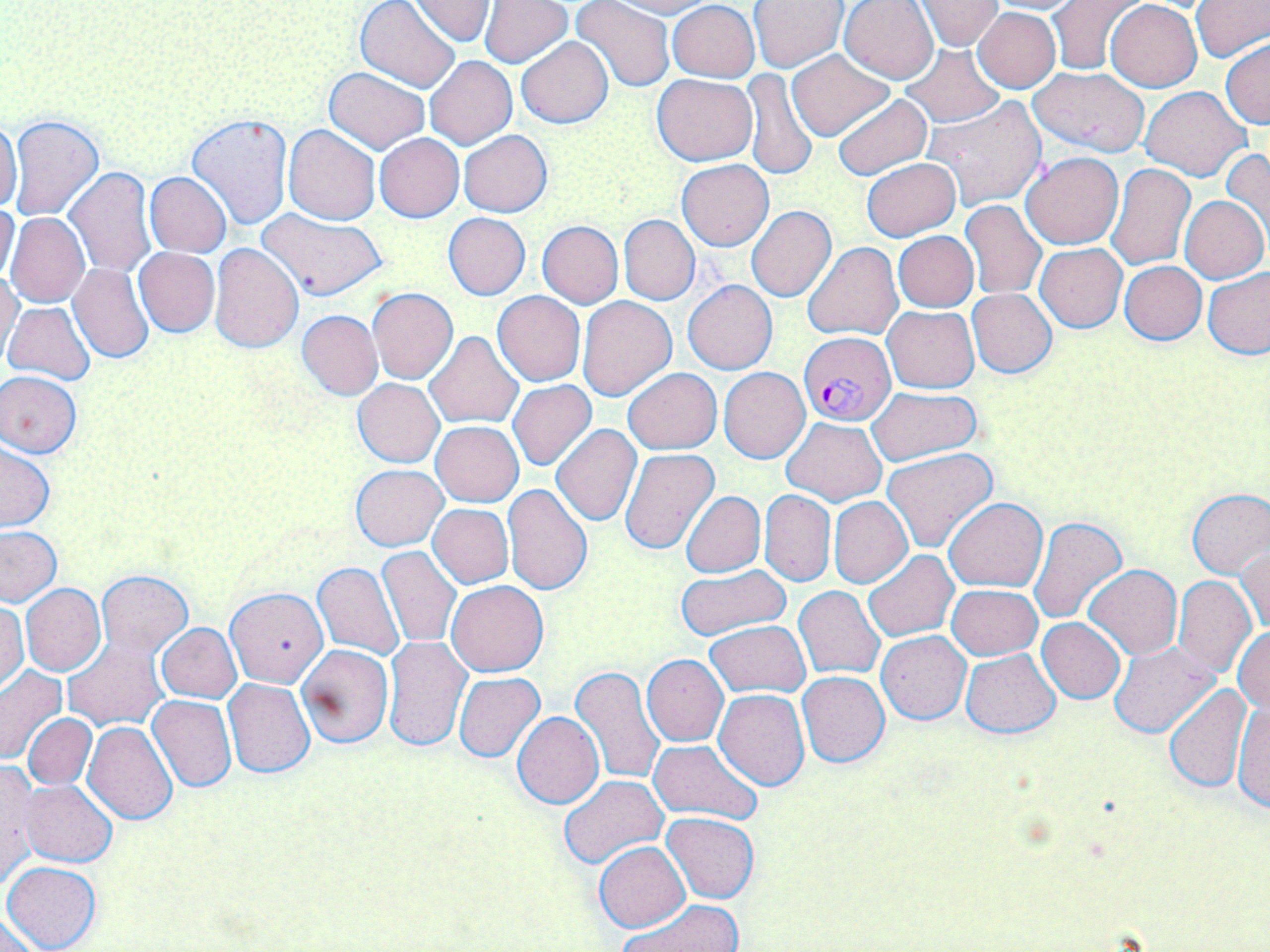

Approximate bounding boxes as [x1, y1, x2, y2] in pixels. Uninfected red blood cell locations: [479, 0, 572, 68], [605, 0, 714, 18], [915, 0, 1004, 50], [1049, 0, 1141, 73], [1105, 0, 1201, 91], [355, 1, 461, 91], [410, 1, 495, 46], [571, 1, 676, 93], [668, 1, 760, 81], [749, 1, 847, 72], [839, 1, 939, 84], [979, 1, 1088, 15], [1190, 1, 1270, 64], [973, 8, 1061, 92], [517, 37, 614, 129], [1221, 39, 1270, 129], [897, 44, 1004, 126], [787, 51, 893, 140], [425, 56, 517, 149], [1029, 67, 1150, 157], [324, 68, 430, 153], [741, 69, 816, 181], [653, 74, 756, 166], [1139, 86, 1251, 181], [832, 93, 931, 181], [923, 96, 1046, 211], [187, 113, 292, 229], [7, 115, 103, 221], [0, 116, 22, 214], [283, 124, 381, 226], [459, 130, 551, 217], [375, 134, 464, 222], [1221, 148, 1270, 245], [1020, 151, 1124, 250], [862, 157, 960, 241], [677, 159, 774, 251], [1107, 162, 1194, 270], [64, 167, 155, 276], [145, 172, 231, 257], [1181, 196, 1269, 283], [962, 200, 1046, 299], [0, 202, 20, 286], [746, 206, 837, 302], [256, 208, 387, 301], [6, 212, 89, 307], [444, 212, 530, 299], [620, 215, 699, 305], [537, 221, 623, 308], [893, 231, 978, 311], [803, 241, 903, 340], [209, 243, 303, 352], [1035, 243, 1127, 332], [134, 248, 220, 336], [1120, 260, 1206, 345], [69, 264, 154, 363], [1202, 267, 1270, 359], [1, 268, 22, 362], [683, 280, 778, 375], [367, 288, 458, 384], [967, 288, 1056, 378], [493, 291, 586, 385], [578, 295, 678, 401], [3, 301, 96, 386], [883, 306, 978, 392], [296, 310, 382, 400], [423, 332, 522, 427], [719, 367, 810, 463], [623, 368, 722, 453], [0, 371, 82, 457], [354, 379, 444, 468], [508, 380, 596, 471], [867, 386, 982, 468], [781, 417, 887, 505], [431, 421, 523, 506], [551, 424, 642, 525], [0, 444, 54, 531], [621, 447, 720, 555], [885, 449, 999, 552], [351, 465, 447, 550], [544, 466, 633, 575], [502, 484, 592, 597], [1186, 488, 1270, 578], [760, 490, 835, 586], [680, 491, 765, 577], [944, 496, 1047, 592], [829, 497, 911, 587], [428, 504, 513, 587], [1028, 515, 1128, 624], [0, 527, 62, 605], [1238, 543, 1269, 638], [379, 546, 461, 648], [863, 551, 958, 642], [314, 562, 404, 659], [1084, 564, 1181, 659], [675, 565, 790, 640], [97, 571, 192, 655], [1084, 572, 1199, 732], [1172, 575, 1256, 678], [447, 580, 549, 677], [21, 584, 106, 676], [948, 584, 1042, 660], [793, 586, 884, 678], [226, 587, 330, 687], [0, 600, 28, 691], [1037, 618, 1126, 703], [705, 621, 810, 697], [156, 624, 241, 702], [1234, 627, 1269, 715], [877, 631, 971, 723], [383, 636, 471, 751], [64, 637, 168, 729], [1108, 641, 1220, 737], [296, 643, 393, 748], [961, 649, 1060, 738], [642, 654, 728, 746], [0, 667, 68, 765], [570, 667, 664, 786], [797, 671, 891, 767], [454, 673, 546, 763], [223, 679, 315, 777], [1164, 683, 1253, 793], [714, 689, 810, 791], [148, 695, 237, 791], [1232, 696, 1270, 814], [513, 712, 604, 809], [23, 713, 96, 789], [84, 722, 178, 824], [649, 739, 763, 824], [0, 761, 39, 886], [559, 773, 668, 868], [22, 780, 117, 867], [662, 812, 760, 903], [595, 828, 755, 915], [594, 842, 690, 931], [2, 861, 101, 951], [616, 899, 745, 952], [1, 913, 43, 952]. Plasmodium falciparum-infected red blood cell locations: [799, 331, 896, 426]. Slide-level diagnosis: Plasmodium falciparum. Thin blood film. One field of a larger specimen. Light microscopy. Captured at 1000x magnification. May-Grünwald-Giemsa stain. Image is 1270×952 pixels.